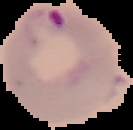
Summary:
  - Result: malaria parasites identified
  - Preparation: thin blood smear
  - Image type: segmented cell region on a black background
  - Image size: 133×130 pixels